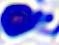
Captured at 400x magnification. A white blood cell is seen. Photomicrograph.